Give the extent of all Plasmodium falciparum-infected red blood cells.
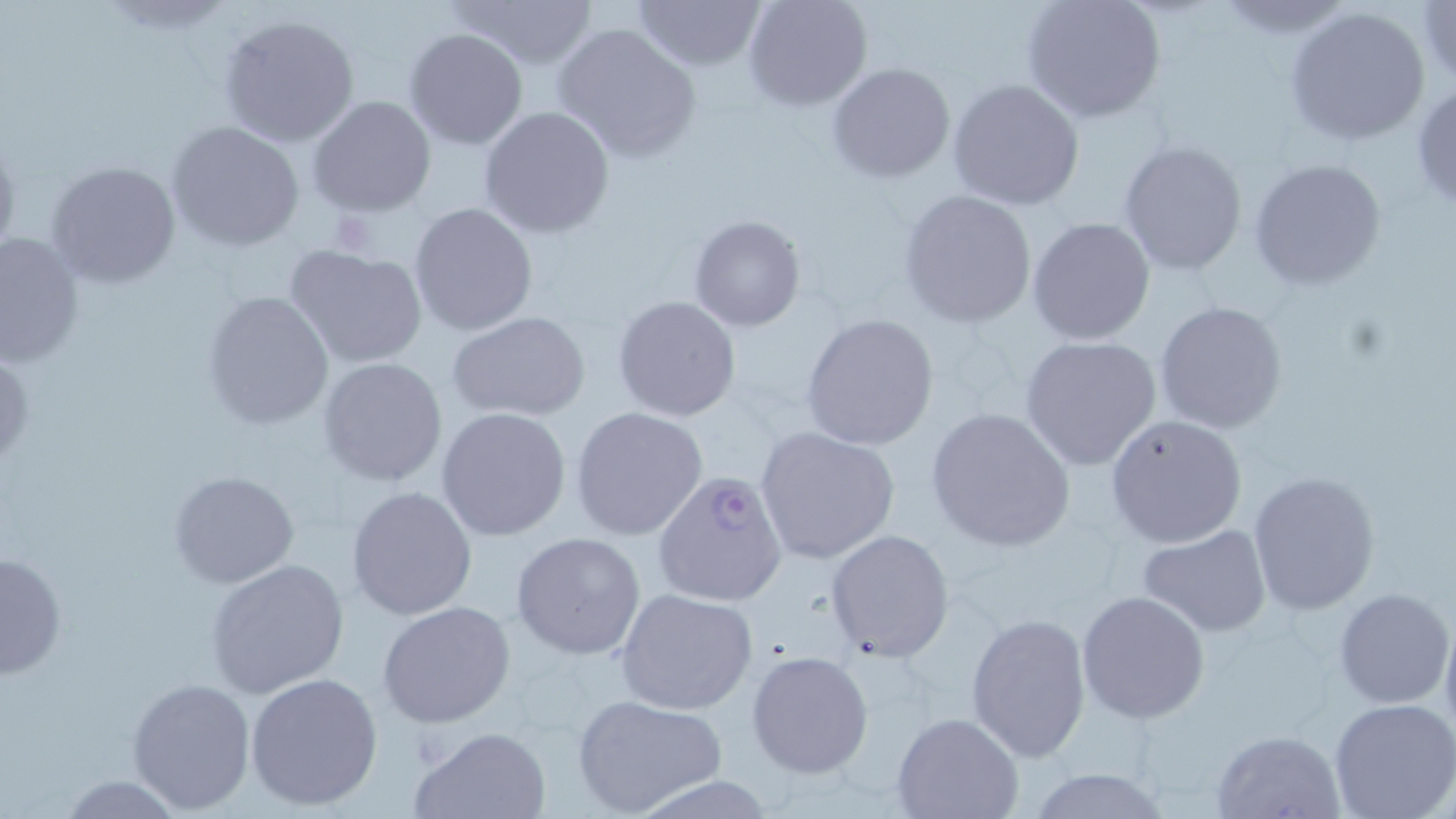
Approximate bounding boxes as named x1/y1/x2/y2 corners in pixels.
Plasmodium falciparum-infected red blood cells: (x1=653, y1=469, x2=788, y2=609).

slide-level diagnosis = Plasmodium falciparum
preparation = thin blood smear
image size = 1456×819 pixels
modality = light microscopy
uninfected red blood cell locations = approximate bounding boxes as named x1/y1/x2/y2 corners in pixels: (x1=449, y1=0, x2=600, y2=71), (x1=632, y1=0, x2=766, y2=72), (x1=743, y1=0, x2=873, y2=111), (x1=1020, y1=0, x2=1167, y2=124), (x1=1417, y1=1, x2=1456, y2=87), (x1=1285, y1=5, x2=1432, y2=147), (x1=220, y1=13, x2=361, y2=149), (x1=552, y1=21, x2=702, y2=163), (x1=406, y1=28, x2=527, y2=149), (x1=828, y1=62, x2=956, y2=184), (x1=947, y1=79, x2=1085, y2=211), (x1=1410, y1=79, x2=1456, y2=214), (x1=307, y1=95, x2=437, y2=219), (x1=478, y1=106, x2=615, y2=238), (x1=166, y1=122, x2=305, y2=252), (x1=1118, y1=140, x2=1248, y2=275), (x1=1247, y1=157, x2=1390, y2=292), (x1=45, y1=160, x2=182, y2=289), (x1=897, y1=190, x2=1037, y2=327), (x1=408, y1=202, x2=538, y2=338), (x1=688, y1=214, x2=807, y2=333), (x1=1026, y1=217, x2=1156, y2=345), (x1=0, y1=231, x2=85, y2=372), (x1=285, y1=243, x2=428, y2=369), (x1=202, y1=291, x2=334, y2=431), (x1=612, y1=296, x2=741, y2=422), (x1=1154, y1=299, x2=1288, y2=435), (x1=449, y1=312, x2=589, y2=423), (x1=800, y1=312, x2=939, y2=452), (x1=1020, y1=335, x2=1165, y2=473), (x1=318, y1=356, x2=449, y2=487), (x1=570, y1=406, x2=710, y2=542), (x1=435, y1=407, x2=572, y2=542), (x1=925, y1=407, x2=1075, y2=551), (x1=1105, y1=415, x2=1248, y2=548), (x1=754, y1=427, x2=899, y2=564), (x1=169, y1=470, x2=300, y2=590), (x1=1248, y1=471, x2=1381, y2=617), (x1=347, y1=485, x2=478, y2=620), (x1=1138, y1=525, x2=1273, y2=637), (x1=826, y1=528, x2=954, y2=662), (x1=511, y1=532, x2=646, y2=661), (x1=0, y1=551, x2=66, y2=681), (x1=207, y1=558, x2=349, y2=698), (x1=1334, y1=587, x2=1454, y2=709), (x1=616, y1=588, x2=759, y2=716), (x1=1077, y1=590, x2=1210, y2=724), (x1=377, y1=602, x2=517, y2=729), (x1=1439, y1=611, x2=1456, y2=747), (x1=966, y1=612, x2=1092, y2=762), (x1=746, y1=650, x2=874, y2=777), (x1=245, y1=673, x2=383, y2=811), (x1=126, y1=677, x2=256, y2=812), (x1=571, y1=694, x2=725, y2=817), (x1=1329, y1=698, x2=1456, y2=819), (x1=891, y1=711, x2=1023, y2=819), (x1=410, y1=726, x2=551, y2=819), (x1=1212, y1=729, x2=1348, y2=819), (x1=1023, y1=769, x2=1172, y2=819), (x1=59, y1=774, x2=186, y2=816)
field of view = one of a larger specimen
stain = May-Grünwald-Giemsa
magnification = 1000x